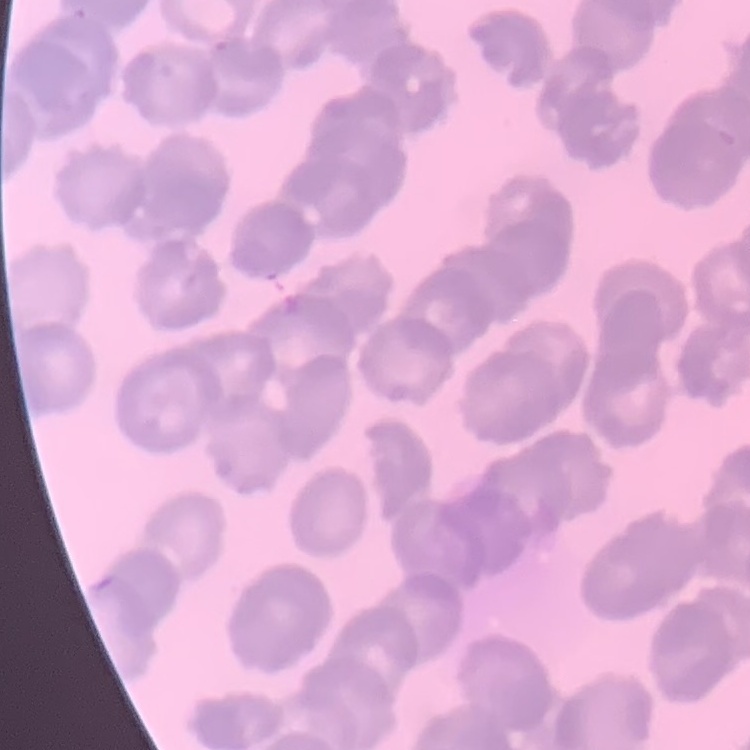

Summary:
  - Red blood cell morphology: rouleaux formation
  - Preparation: thin blood smear
  - Stain: Field's or Giemsa
  - Image type: one tile cut from a larger photomicrograph